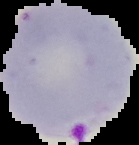
Image is 139×145 pixels. Result: malaria parasites identified. From a thin blood film. Cell region segmented out of the field of view; the surrounding area is masked to black.